Classify this cell by malaria status.
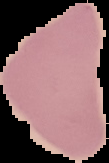
It is uninfected.

image_type: segmented cell region with the area outside set to black
image_size: 109×163 pixels
preparation: thin blood film